Assess the morphology of the red blood cells.
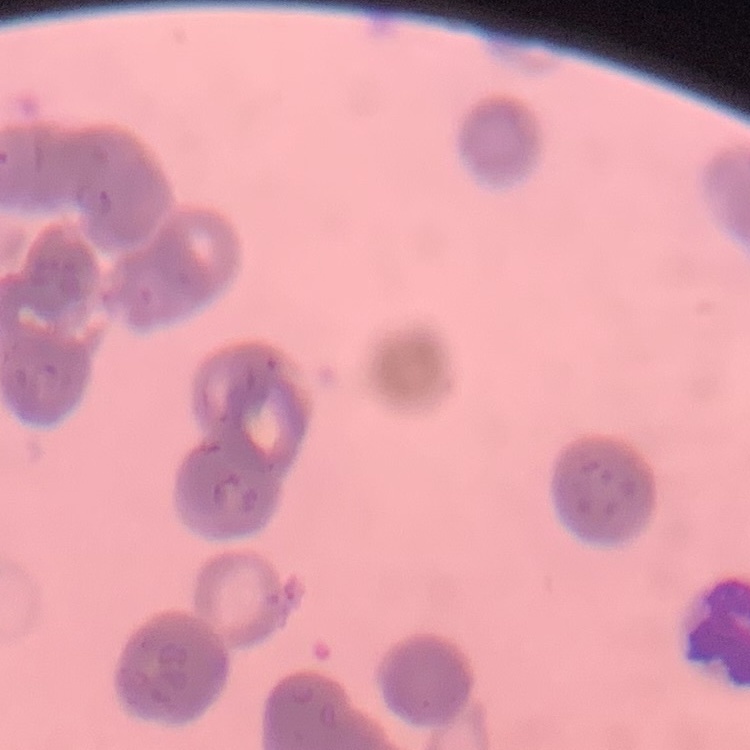
Rouleaux formation.

Thin blood smear. Square crop of a larger photomicrograph. Field's or Giemsa stain.